Locate every blood parasite and identify its species.
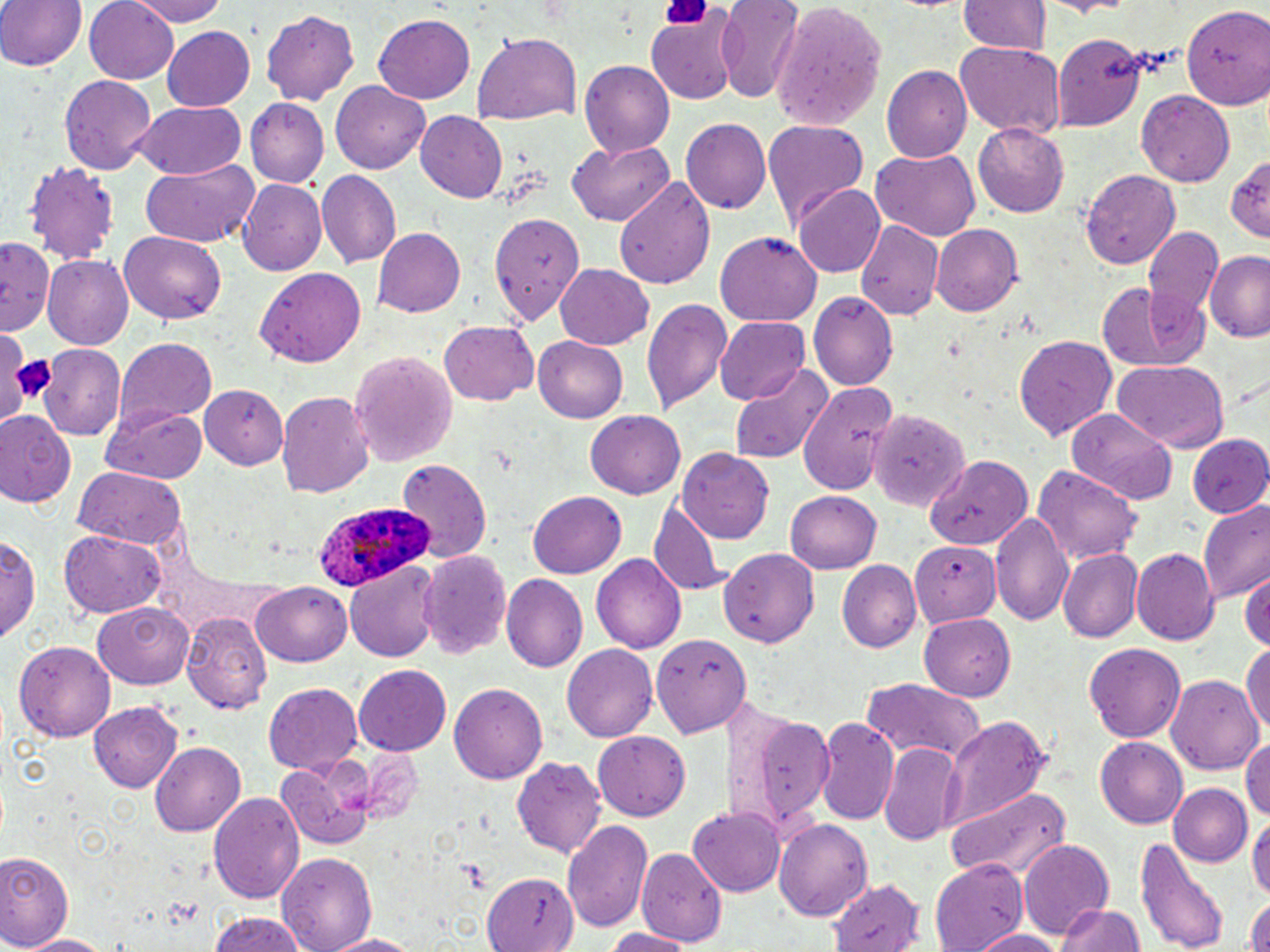

Approximate bounding boxes as (x1, y1, x2, y2) in pixels.
Plasmodium ovale-infected red blood cells: (306, 499, 434, 596).
No Plasmodium falciparum, Plasmodium malariae, Plasmodium vivax, Babesia divergens, or Trypanosoma brucei observed.

Uninfected red blood cell locations: (0, 0, 82, 73), (84, 0, 182, 86), (126, 0, 236, 26), (715, 0, 805, 103), (959, 1, 1050, 56), (1182, 4, 1270, 111), (775, 5, 887, 132), (261, 9, 359, 104), (647, 13, 738, 102), (374, 15, 475, 103), (163, 28, 255, 110), (474, 34, 580, 125), (1054, 34, 1151, 132), (954, 40, 1065, 136), (580, 59, 674, 159), (882, 65, 970, 163), (60, 76, 156, 175), (329, 79, 430, 174), (1135, 91, 1234, 182), (246, 97, 328, 186), (129, 101, 247, 180), (415, 111, 507, 203), (680, 119, 771, 216), (763, 120, 868, 227), (973, 124, 1070, 218), (568, 138, 675, 227), (871, 146, 981, 241), (26, 157, 118, 266), (1226, 160, 1270, 238), (140, 163, 258, 249), (1080, 168, 1188, 273), (315, 170, 400, 268), (613, 175, 718, 289), (237, 180, 327, 277), (795, 184, 886, 279), (488, 211, 588, 321), (856, 220, 942, 320), (931, 222, 1023, 314), (374, 228, 466, 318), (1143, 229, 1224, 329), (122, 231, 228, 325), (716, 231, 820, 327), (0, 236, 56, 330), (1208, 250, 1270, 343), (41, 252, 134, 348), (554, 263, 656, 349), (257, 268, 366, 368), (1096, 280, 1206, 372), (808, 292, 898, 390), (642, 295, 734, 415), (715, 317, 813, 403), (439, 322, 538, 405), (1015, 333, 1119, 440), (113, 335, 218, 424), (533, 336, 627, 423), (40, 346, 125, 439), (350, 349, 458, 464), (1111, 360, 1229, 453), (729, 364, 835, 465), (799, 381, 895, 493), (200, 383, 288, 467), (276, 390, 373, 497), (100, 402, 211, 483), (1067, 409, 1176, 507), (0, 410, 77, 509), (586, 410, 685, 500), (865, 414, 976, 511), (1185, 433, 1270, 517), (676, 450, 774, 543), (928, 454, 1034, 550), (394, 460, 493, 561), (1032, 464, 1143, 561), (73, 468, 187, 549), (527, 491, 626, 578), (785, 491, 880, 573), (648, 500, 727, 597), (1198, 503, 1270, 604), (991, 509, 1073, 625), (59, 529, 169, 619), (0, 531, 42, 644), (914, 541, 1004, 630), (724, 543, 826, 646), (416, 549, 513, 661), (1133, 549, 1220, 645), (1058, 550, 1141, 643), (592, 554, 686, 653), (837, 559, 921, 653), (346, 565, 442, 662), (1243, 570, 1270, 654), (502, 574, 588, 672), (253, 582, 352, 666), (93, 601, 197, 688), (181, 609, 275, 715), (921, 612, 1019, 699), (651, 634, 748, 738), (13, 638, 116, 739), (1241, 638, 1270, 744), (1083, 642, 1187, 742), (562, 644, 657, 744), (354, 666, 451, 757), (1164, 671, 1264, 776), (860, 679, 986, 766), (263, 683, 364, 774), (450, 684, 546, 784), (89, 702, 182, 791), (724, 703, 835, 831), (816, 717, 898, 824), (947, 718, 1051, 830), (593, 732, 690, 821), (1242, 735, 1270, 821), (1095, 737, 1191, 828), (150, 741, 246, 836), (878, 745, 960, 846), (275, 758, 373, 848), (513, 758, 607, 860), (1169, 782, 1252, 866), (947, 785, 1074, 885), (206, 790, 304, 903), (688, 805, 786, 896), (1248, 811, 1270, 906), (562, 819, 652, 932), (774, 820, 873, 922), (1137, 834, 1233, 952), (1017, 839, 1114, 938), (637, 847, 727, 946), (0, 850, 74, 951), (277, 851, 376, 952), (929, 859, 1028, 952), (481, 874, 572, 950), (825, 877, 923, 950), (1244, 897, 1270, 952), (1056, 900, 1144, 952), (206, 911, 314, 952), (601, 926, 695, 952), (971, 927, 1071, 952), (18, 932, 112, 950), (321, 932, 427, 951). Platelet locations: (660, 0, 712, 27), (13, 353, 61, 398). Slide-level diagnosis: Plasmodium ovale. Captured at 1000x magnification. One field of a larger specimen. Light microscopy. Image is 1270×952 pixels. Thin blood film. May-Grünwald-Giemsa stain.